Name the blood parasite species.
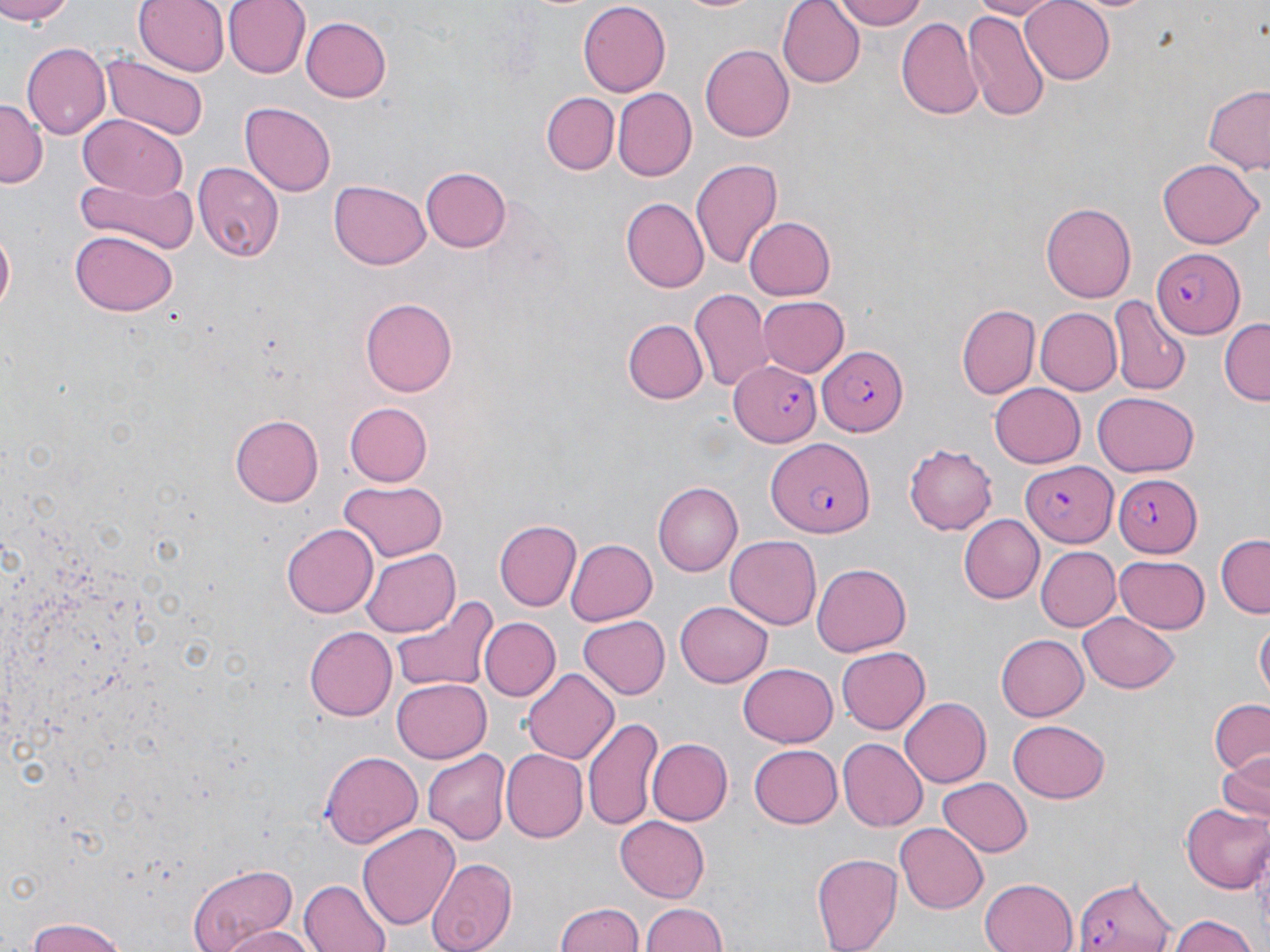

Plasmodium falciparum.

Summary:
  - Coordinate format: approximate bounding boxes as [x1, y1, x2, y2] in pixels
  - Plasmodium falciparum-infected red blood cell locations: [1152, 250, 1244, 338], [814, 337, 910, 439], [727, 360, 821, 445], [766, 441, 873, 540], [1022, 463, 1117, 547], [1111, 475, 1202, 556], [1072, 874, 1179, 952]
  - Uninfected red blood cell locations: [0, 0, 75, 24], [135, 0, 229, 76], [222, 0, 310, 79], [776, 0, 864, 88], [836, 0, 927, 29], [970, 0, 1062, 19], [1020, 0, 1115, 83], [579, 1, 670, 94], [672, 1, 769, 16], [960, 8, 1050, 123], [300, 16, 393, 103], [896, 17, 984, 120], [23, 43, 111, 139], [699, 44, 796, 142], [100, 52, 207, 139], [1200, 85, 1270, 174], [613, 88, 697, 181], [542, 92, 618, 173], [0, 97, 47, 184], [239, 102, 336, 198], [78, 115, 186, 199], [691, 158, 783, 271], [1158, 159, 1262, 249], [194, 162, 285, 263], [421, 166, 512, 251], [77, 172, 197, 256], [329, 179, 431, 272], [621, 197, 709, 292], [1041, 201, 1135, 303], [743, 215, 836, 302], [0, 220, 16, 318], [70, 232, 178, 316], [690, 289, 773, 395], [757, 295, 849, 378], [1110, 295, 1191, 397], [360, 298, 456, 397], [958, 304, 1040, 398], [1034, 306, 1120, 394], [1219, 318, 1270, 403], [622, 319, 707, 405], [989, 382, 1086, 468], [1093, 389, 1199, 476], [344, 402, 432, 486], [231, 411, 324, 504], [905, 444, 998, 533], [338, 480, 449, 562], [655, 482, 747, 577], [959, 516, 1044, 603], [494, 519, 581, 611], [283, 524, 378, 618], [1216, 535, 1270, 617], [724, 537, 820, 630], [564, 538, 657, 626], [1038, 546, 1120, 631], [361, 549, 459, 634], [1114, 553, 1210, 632], [813, 562, 910, 657], [391, 591, 499, 694], [675, 600, 772, 687], [1080, 614, 1179, 694], [578, 616, 670, 700], [478, 617, 559, 702], [1255, 621, 1268, 703], [306, 625, 400, 720], [994, 634, 1088, 722], [837, 646, 929, 732], [739, 663, 837, 746], [522, 668, 620, 763], [392, 679, 491, 762], [899, 697, 991, 788], [1209, 699, 1269, 779], [585, 716, 664, 833], [1009, 719, 1111, 804], [645, 737, 733, 827], [836, 739, 926, 831], [749, 744, 843, 829], [422, 748, 510, 845], [502, 750, 587, 842], [1215, 750, 1269, 825], [320, 752, 423, 848], [938, 776, 1032, 857], [1183, 803, 1270, 895], [615, 816, 712, 901], [896, 821, 989, 914], [358, 824, 460, 929], [811, 851, 900, 952], [425, 856, 518, 952], [186, 863, 300, 952], [979, 876, 1079, 952], [299, 879, 393, 952], [554, 901, 645, 952], [640, 903, 730, 952], [1166, 914, 1264, 952], [20, 919, 132, 952], [224, 925, 313, 952]
  - Field of view: single
  - Image size: 1270×952 pixels
  - Stain: May-Grünwald-Giemsa
  - Preparation: thin blood smear
  - Modality: light microscopy
  - Magnification: 1000x